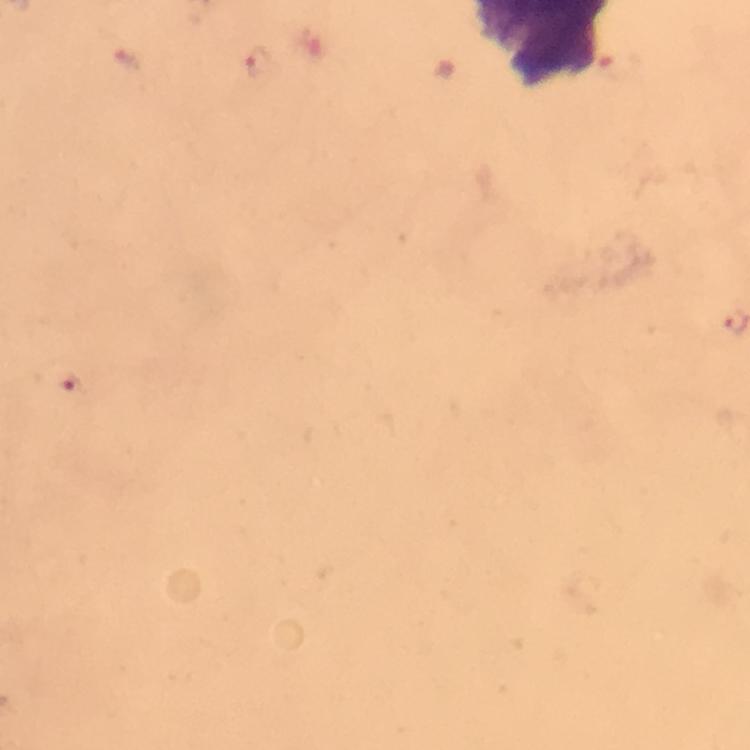

context = from a malaria diagnostic workup
image size = 750×750 pixels
cropped from = a single field of view
magnification = 100x
malaria parasite locations = approximate object centers, in pixels from the top-left corner: (x=68, y=390)
immersion oil = used
stain = Giemsa
capture = smartphone photograph through a microscope
preparation = thick smear